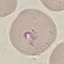

Summary:
  - Result: malaria parasites detected
  - Image type: cell patch, automatically extracted from a larger field of view and resized to 64 × 64 pixels
  - Stain: Giemsa
  - Preparation: thin smear
  - Capture: smartphone camera at the microscope eyepiece